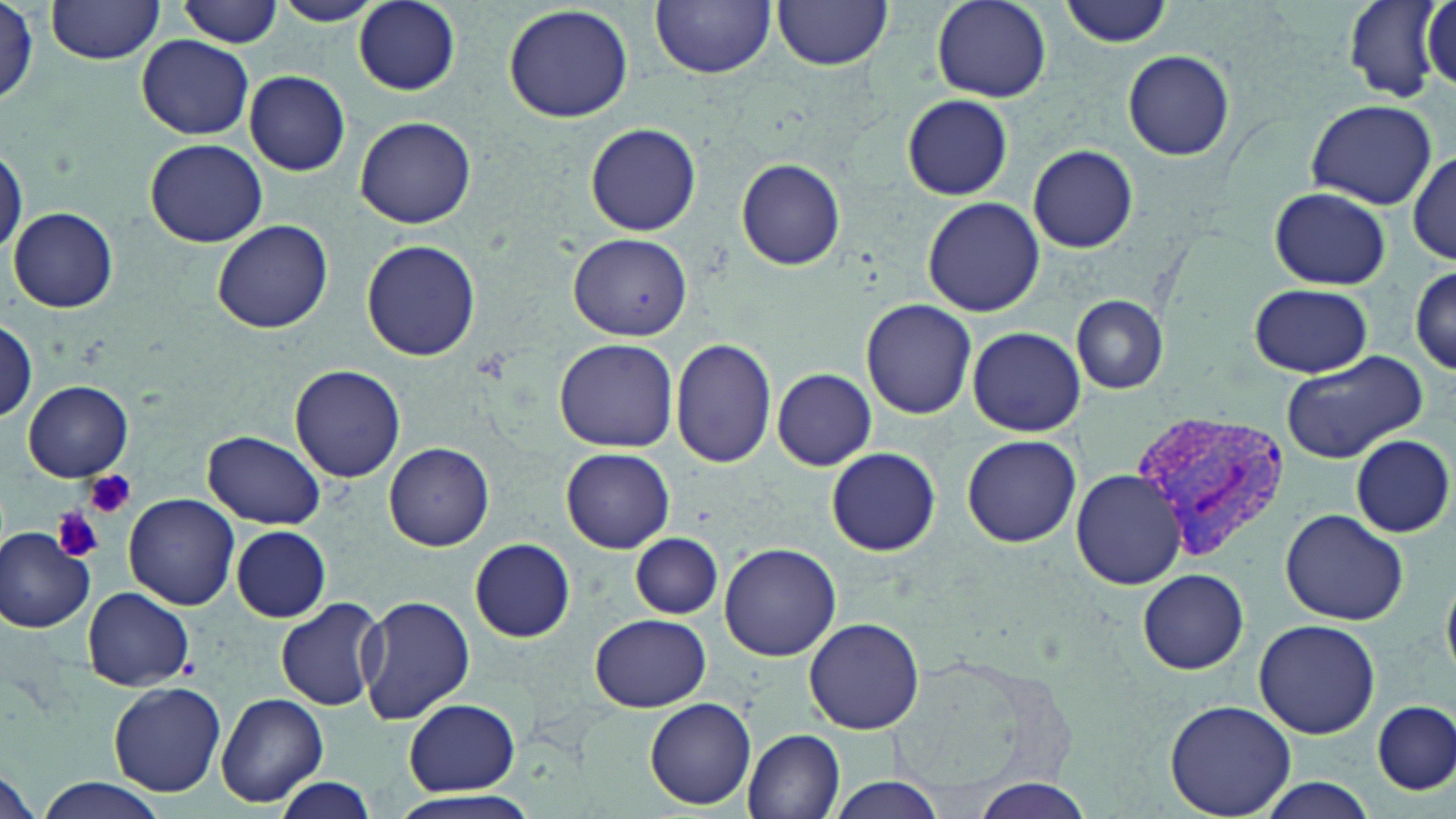

slide-level diagnosis = Plasmodium vivax
image size = 1456×819 pixels
stain = May-Grünwald-Giemsa
modality = optical microscopy
uninfected red blood cell locations = approximate bounding boxes as [x1, y1, x2, y2] in pixels: [45, 0, 166, 64], [179, 0, 284, 47], [272, 0, 385, 26], [353, 0, 460, 94], [652, 0, 774, 78], [930, 0, 1051, 103], [1059, 0, 1173, 47], [771, 1, 893, 71], [1344, 1, 1447, 102], [503, 4, 633, 123], [1, 6, 41, 108], [136, 36, 254, 139], [1123, 50, 1235, 160], [243, 71, 351, 176], [902, 94, 1013, 200], [1305, 100, 1435, 208], [354, 115, 476, 229], [585, 122, 702, 236], [145, 138, 267, 246], [0, 143, 25, 256], [1028, 144, 1139, 253], [1410, 150, 1455, 262], [736, 158, 844, 271], [1268, 186, 1391, 290], [920, 197, 1046, 317], [8, 206, 118, 311], [212, 219, 332, 332], [571, 233, 692, 342], [362, 241, 481, 361], [1410, 265, 1455, 373], [1249, 281, 1373, 378], [1069, 295, 1170, 395], [860, 299, 978, 420], [0, 320, 39, 422], [967, 326, 1086, 437], [554, 338, 679, 454], [670, 338, 777, 468], [1279, 347, 1429, 464], [290, 364, 406, 482], [772, 368, 876, 470], [23, 380, 132, 481], [203, 430, 327, 527], [1350, 433, 1454, 538], [960, 434, 1082, 548], [385, 441, 495, 550], [825, 447, 941, 556], [562, 448, 674, 552], [1069, 469, 1186, 591], [123, 492, 240, 610], [1280, 507, 1409, 626], [231, 527, 329, 622], [0, 528, 95, 632], [631, 533, 721, 620], [469, 539, 575, 642], [718, 541, 840, 661], [1136, 568, 1249, 674], [84, 587, 194, 689], [359, 595, 475, 723], [276, 597, 386, 712], [591, 614, 711, 711], [805, 616, 923, 734], [1253, 618, 1382, 739], [110, 682, 226, 796], [215, 692, 328, 806], [645, 696, 756, 810], [405, 698, 521, 795], [1374, 699, 1455, 795], [1163, 700, 1299, 819], [743, 729, 846, 818], [1, 770, 41, 819], [34, 777, 163, 818], [274, 778, 378, 818], [824, 778, 949, 818], [1250, 779, 1383, 817], [971, 780, 1093, 817], [384, 791, 542, 817]
magnification = 1000x
preparation = thin blood smear
field of view = single
platelet locations = approximate bounding boxes as [x1, y1, x2, y2] in pixels: [82, 470, 136, 519], [54, 506, 106, 562]
Plasmodium vivax-infected red blood cell locations = approximate bounding boxes as [x1, y1, x2, y2] in pixels: [1128, 413, 1291, 563]